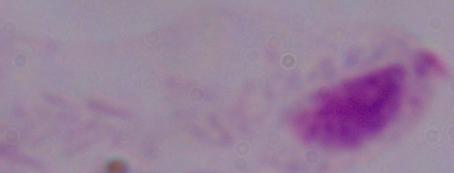

A trichomonad is seen. Micrograph. 1000x magnification.